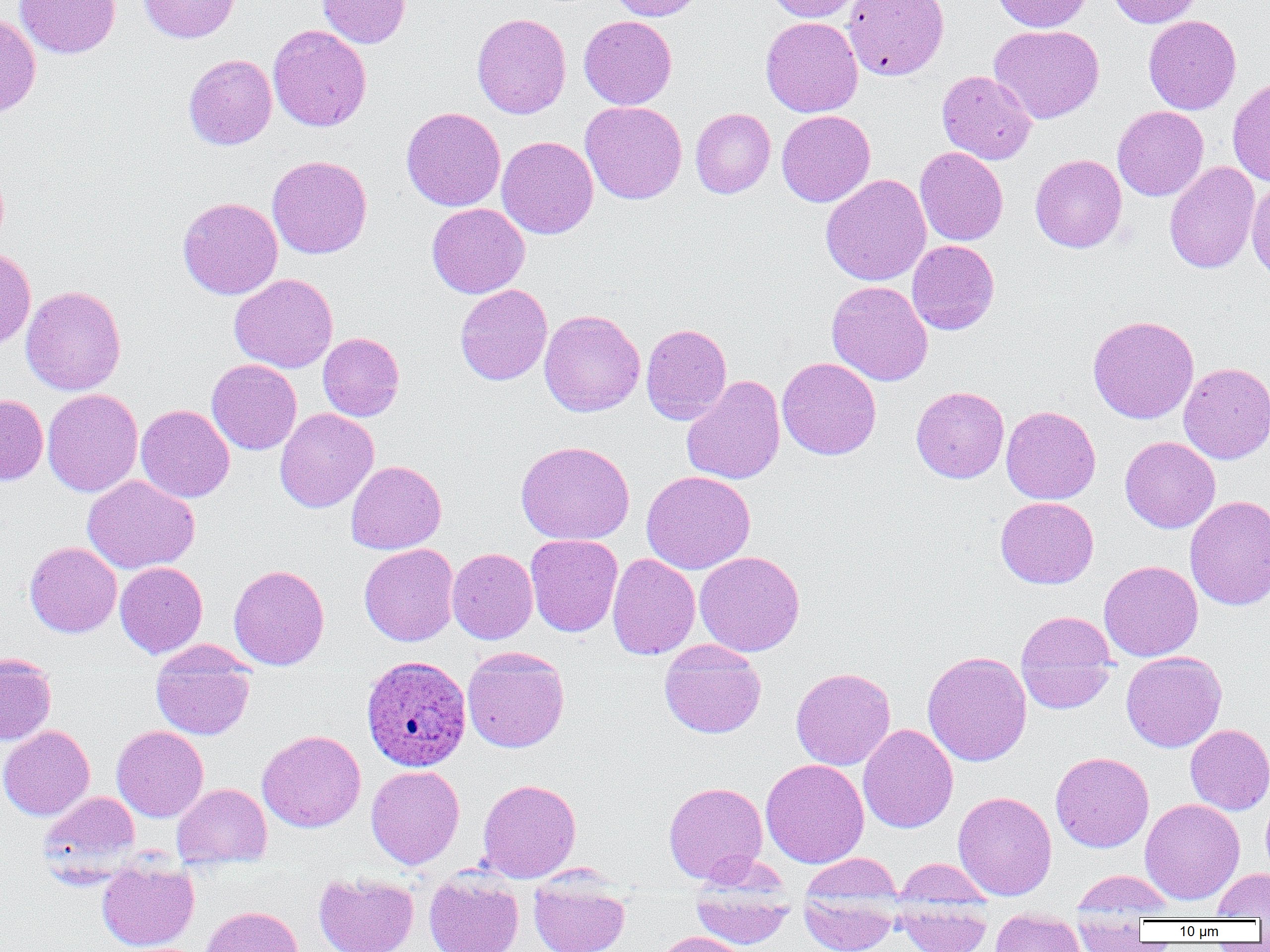
Summary:
  - Coordinate format: approximate bounding boxes as (x1, y1, x2, y2) in pixels
  - Plasmodium ovale-infected red blood cell locations: (361, 655, 472, 772)
  - Uninfected red blood cell locations: (13, 0, 121, 59), (139, 0, 239, 43), (317, 0, 411, 48), (608, 0, 704, 21), (765, 0, 863, 22), (842, 0, 949, 80), (992, 0, 1092, 32), (1106, 0, 1203, 28), (471, 12, 572, 119), (0, 13, 41, 118), (1143, 15, 1241, 115), (579, 16, 677, 109), (760, 16, 863, 117), (268, 24, 372, 132), (988, 24, 1105, 124), (184, 54, 277, 150), (936, 70, 1038, 165), (1227, 77, 1270, 186), (580, 101, 687, 204), (1112, 106, 1209, 201), (401, 107, 505, 211), (690, 107, 776, 198), (776, 110, 875, 207), (496, 136, 598, 239), (915, 146, 1008, 246), (1030, 153, 1127, 253), (267, 155, 372, 259), (1164, 161, 1260, 274), (821, 174, 931, 286), (1247, 179, 1270, 283), (177, 196, 283, 299), (426, 203, 530, 298), (907, 240, 1000, 335), (0, 248, 36, 350), (229, 273, 338, 372), (827, 281, 933, 386), (455, 284, 552, 385), (20, 285, 126, 396), (539, 309, 645, 417), (1088, 315, 1198, 424), (641, 323, 732, 424), (317, 332, 405, 421), (777, 357, 882, 459), (207, 359, 302, 455), (1179, 362, 1270, 464), (681, 374, 785, 485), (911, 386, 1009, 483), (42, 389, 143, 497), (0, 394, 48, 485), (136, 404, 235, 503), (1001, 405, 1101, 504), (275, 408, 378, 512), (1120, 436, 1220, 533), (515, 441, 635, 545), (346, 460, 447, 554), (641, 470, 756, 575), (83, 475, 200, 574), (1185, 495, 1270, 610), (995, 496, 1098, 589), (525, 534, 623, 637), (24, 541, 122, 638), (359, 543, 459, 646), (447, 548, 538, 644), (694, 551, 805, 656), (607, 553, 700, 660), (1099, 560, 1203, 661), (115, 562, 208, 658), (228, 564, 330, 670), (1015, 611, 1117, 712), (659, 638, 766, 738), (151, 643, 257, 740), (462, 646, 570, 752), (922, 650, 1032, 766), (1121, 651, 1226, 752), (0, 653, 57, 745), (790, 667, 896, 770), (858, 723, 958, 833), (1185, 724, 1270, 815), (0, 725, 94, 820), (112, 725, 208, 822), (257, 729, 366, 833), (1050, 751, 1154, 853), (760, 758, 869, 868), (366, 765, 465, 869), (477, 778, 581, 882), (663, 781, 768, 883), (173, 783, 271, 866), (38, 791, 140, 875), (953, 791, 1057, 900), (1140, 798, 1245, 905), (894, 858, 994, 907), (96, 859, 199, 952), (1212, 868, 1270, 920), (1070, 869, 1175, 915), (314, 872, 419, 952), (424, 872, 524, 952), (797, 873, 901, 952), (529, 874, 630, 952), (689, 884, 795, 951), (893, 900, 992, 952), (199, 905, 304, 952), (989, 910, 1085, 952), (1072, 921, 1152, 951), (654, 931, 752, 952)
  - Slide-level diagnosis: Plasmodium ovale
  - Modality: light microscopy
  - Preparation: thin blood smear
  - Field of view: one of a larger specimen
  - Image size: 1270×952 pixels
  - Magnification: 1000x